Name the cell type shown.
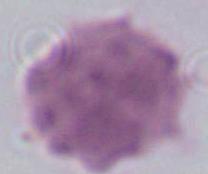
An erythrocyte.

magnification = 1000x
modality = micrograph